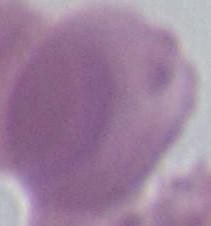

Summary:
  - Modality: photomicrograph
  - Identification: red blood cell
  - Magnification: 1000x